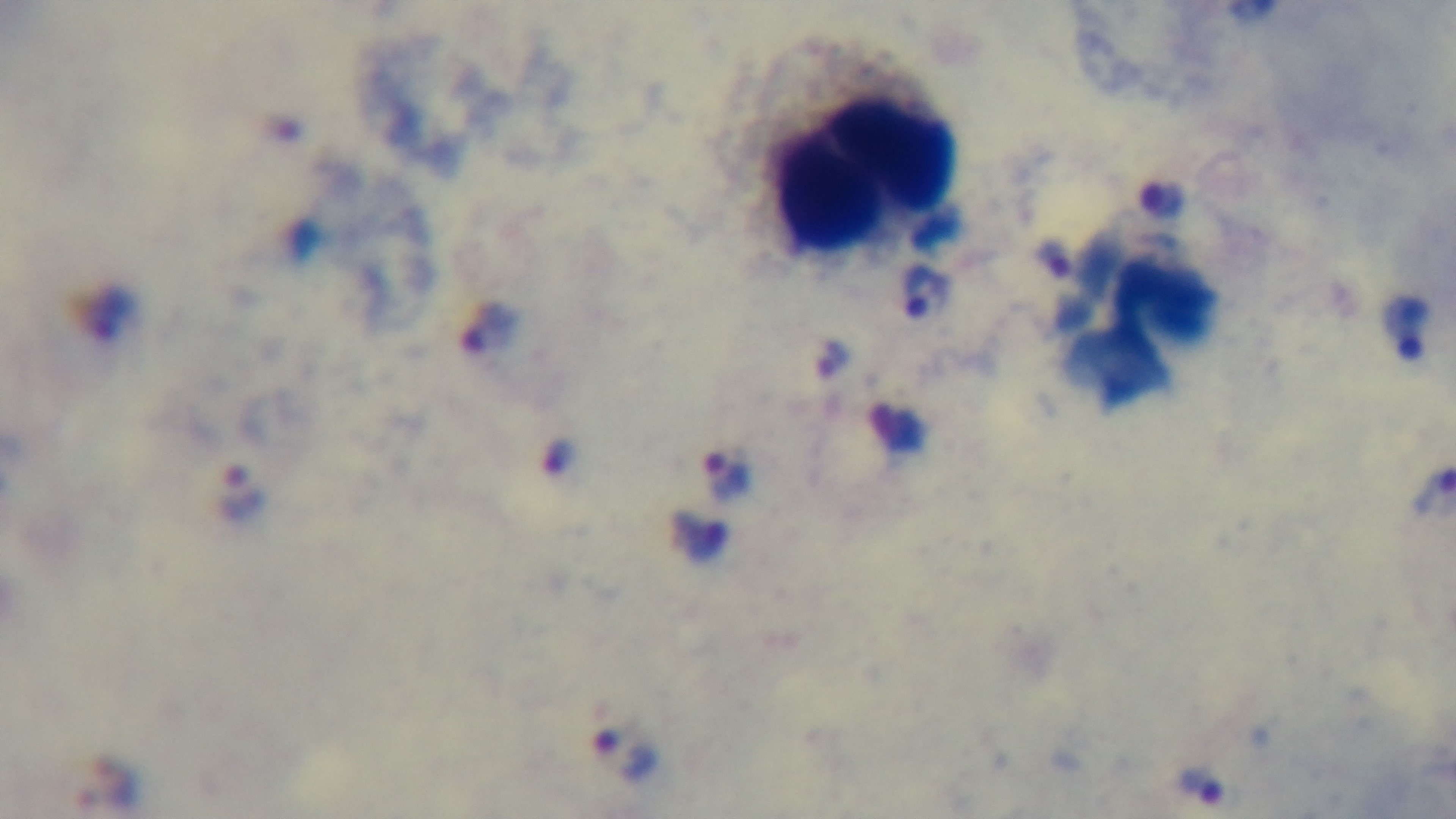
Malaria status: infected. Preparation: thick blood film. Mounted 4K digital camera. Single field of view. Photomicrograph. Giemsa-stained. 100x oil-immersion objective.